Outline each blood parasite and name the species.
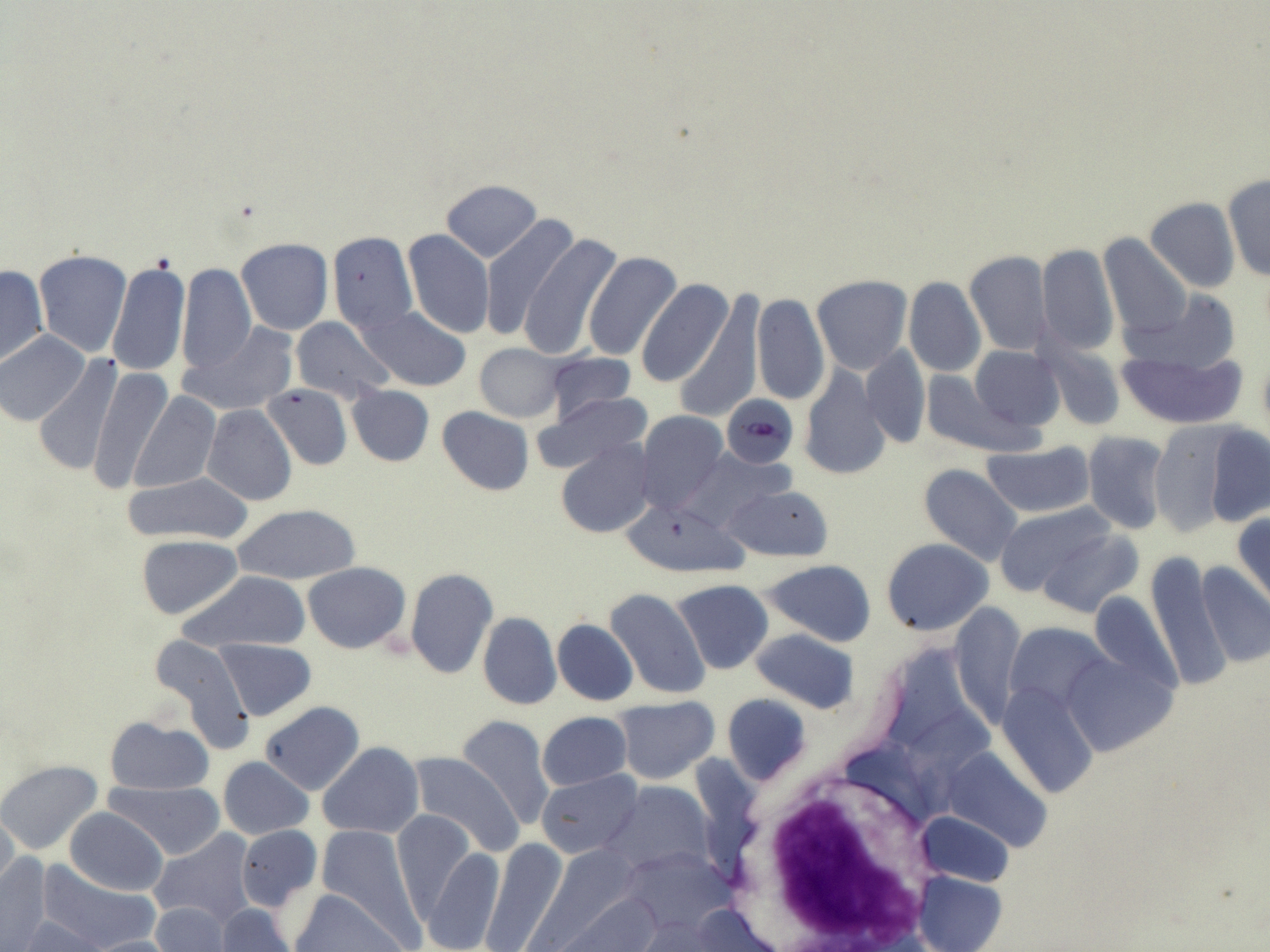

Approximate bounding boxes as (x1, y1, x2, y2) in pixels.
Plasmodium falciparum-infected red blood cells: (722, 394, 797, 469).
No Plasmodium ovale, Plasmodium malariae, Plasmodium vivax, Babesia divergens, or Trypanosoma brucei observed.

Summary:
  - White blood cell locations: (745, 763, 944, 944)
  - Uninfected red blood cell locations: (1222, 174, 1270, 282), (442, 180, 543, 261), (1145, 198, 1240, 293), (481, 216, 583, 342), (403, 229, 494, 338), (328, 231, 418, 333), (516, 234, 622, 361), (1099, 234, 1192, 338), (236, 239, 333, 335), (1036, 243, 1119, 357), (33, 250, 132, 358), (583, 251, 681, 362), (963, 252, 1053, 357), (106, 259, 190, 378), (0, 263, 48, 369), (176, 263, 256, 377), (812, 275, 912, 375), (903, 277, 986, 378), (637, 279, 736, 389), (674, 289, 763, 424), (751, 292, 828, 407), (357, 307, 471, 391), (290, 316, 396, 402), (1111, 317, 1252, 429), (184, 321, 297, 415), (0, 330, 90, 426), (1037, 340, 1128, 431), (476, 343, 563, 421), (965, 344, 1065, 434), (859, 345, 931, 449), (544, 351, 637, 424), (33, 355, 122, 481), (87, 366, 174, 494), (919, 366, 1035, 458), (797, 367, 891, 480), (262, 384, 352, 470), (347, 386, 434, 466), (128, 388, 221, 493), (536, 391, 653, 478), (202, 404, 296, 507), (438, 407, 534, 496), (635, 411, 728, 515), (1195, 422, 1269, 528), (1149, 423, 1240, 538), (1080, 432, 1170, 534), (555, 440, 655, 538), (982, 442, 1094, 519), (677, 448, 795, 532), (917, 465, 1022, 567), (123, 473, 254, 544), (723, 484, 834, 561), (622, 500, 747, 577), (993, 503, 1126, 602), (232, 504, 361, 585), (1233, 507, 1270, 616), (1034, 528, 1143, 619), (136, 535, 244, 620), (882, 539, 993, 637), (1146, 552, 1231, 694), (762, 560, 877, 646), (303, 562, 411, 654), (1194, 562, 1270, 670), (405, 569, 497, 678), (182, 571, 310, 652), (671, 579, 774, 674), (605, 588, 711, 700), (950, 603, 1026, 729), (477, 611, 561, 710), (552, 620, 638, 706), (750, 630, 861, 714), (148, 635, 256, 756), (213, 638, 318, 721), (880, 644, 970, 754), (997, 681, 1101, 798), (722, 694, 811, 786), (611, 698, 719, 785), (258, 701, 364, 796), (909, 701, 1006, 803), (537, 712, 631, 791), (455, 715, 556, 829), (104, 716, 211, 795), (319, 742, 424, 837), (939, 749, 1055, 855), (407, 754, 522, 856), (217, 756, 313, 839), (0, 760, 102, 854), (537, 770, 643, 860), (105, 780, 225, 860), (603, 782, 714, 876), (0, 808, 21, 898), (64, 808, 168, 896), (391, 810, 476, 923), (913, 810, 1014, 886), (315, 823, 422, 939), (235, 825, 322, 912), (148, 830, 256, 928), (480, 839, 569, 952), (422, 844, 504, 952), (617, 846, 736, 936), (0, 853, 54, 950), (36, 863, 159, 950), (914, 872, 1006, 952), (288, 885, 408, 951), (559, 894, 664, 952), (149, 901, 234, 951), (214, 903, 297, 952), (681, 904, 782, 951), (14, 915, 104, 951), (79, 935, 184, 952)
  - Slide-level diagnosis: Plasmodium falciparum
  - Modality: optical microscopy
  - Field of view: single
  - Preparation: thin blood film
  - Image size: 1270×952 pixels
  - Stain: May-Grünwald-Giemsa
  - Magnification: 1000x